Identify the parasite.
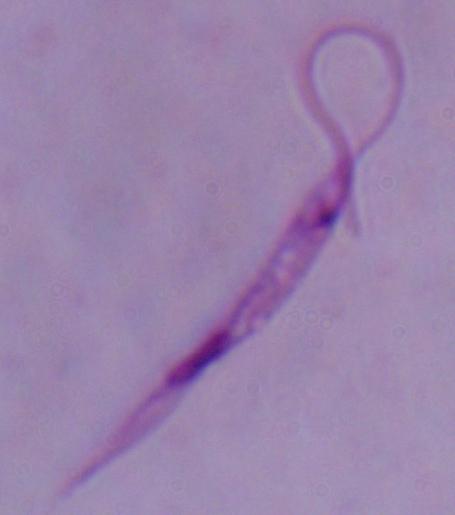
This is Leishmania.

Summary:
  - Magnification: 1000x
  - Modality: photomicrograph